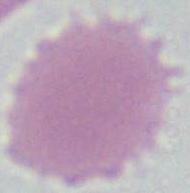

Summary:
  - Modality: photomicrograph
  - Magnification: 1000x
  - Identification: red blood cell